Look for Plasmodium parasites.
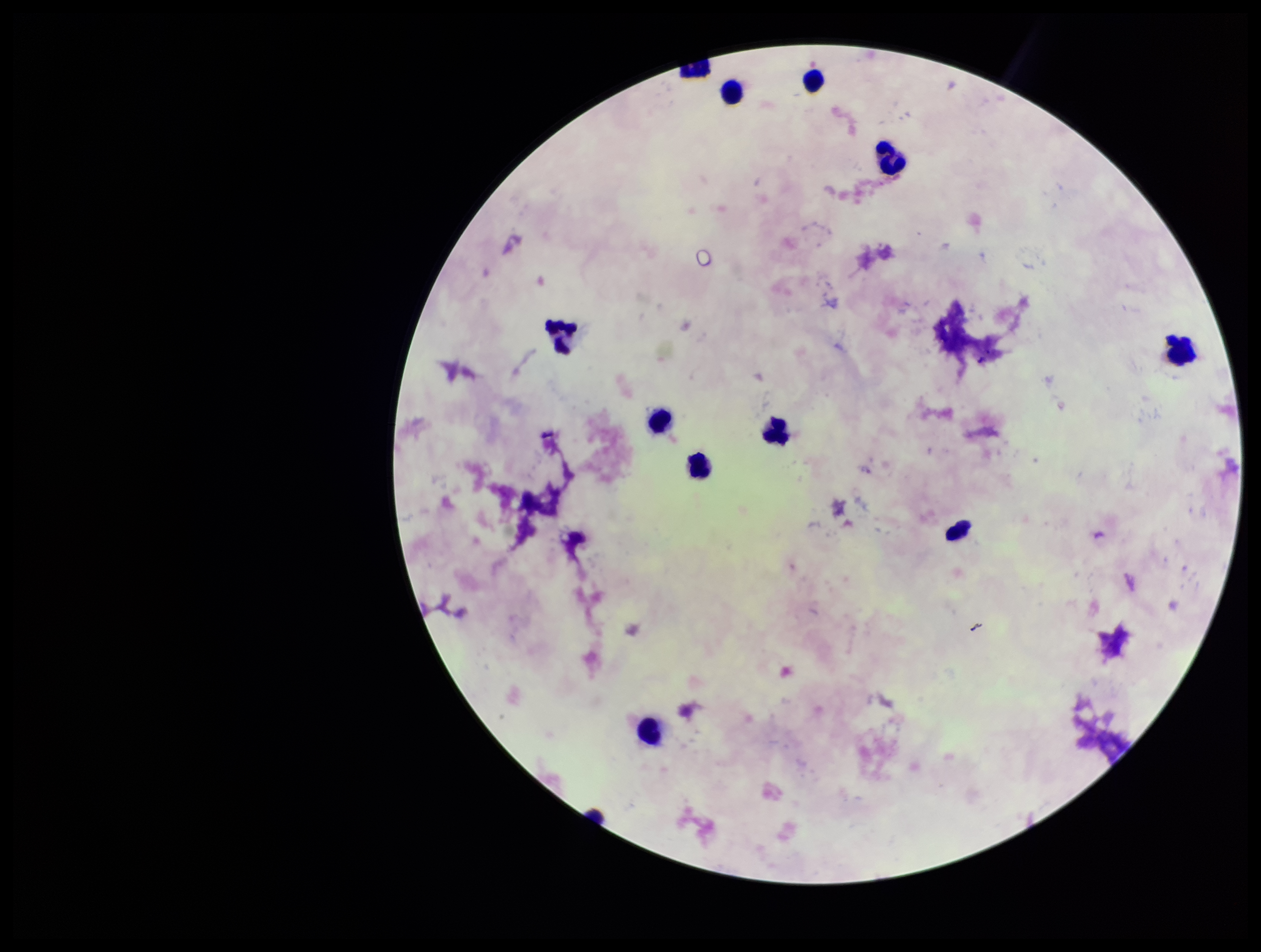

None identified.

{
  "leukocyte_count": 11,
  "field_of_view": "single",
  "image_size": "1261×952 pixels",
  "patient_malaria_status": "negative",
  "stain": "Giemsa",
  "capture": "smartphone photograph through the microscope eyepiece",
  "parasite_count": 0,
  "preparation": "thick"
}